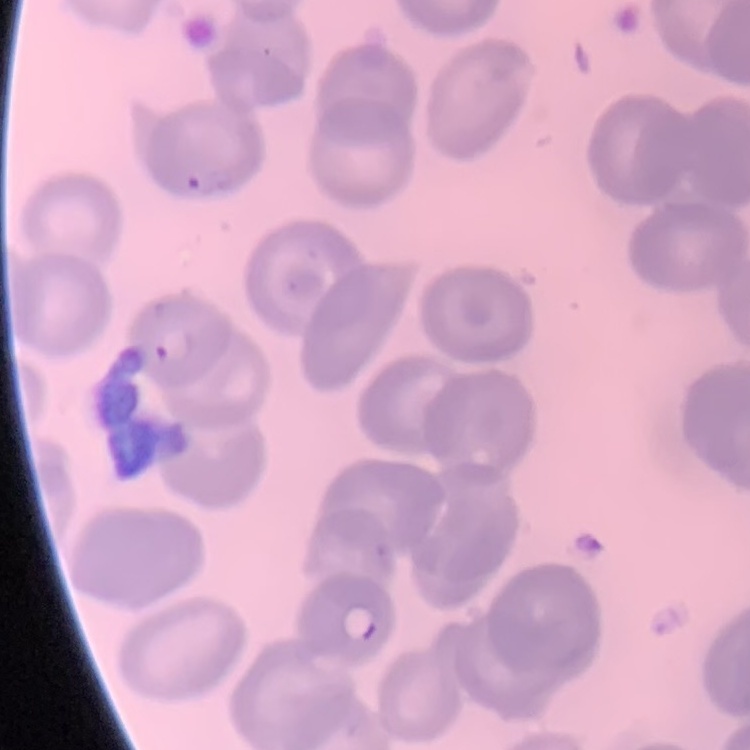
red blood cell morphology = no rouleaux formation
preparation = thin blood smear
stain = Field's or Giemsa
image type = square crop of a larger photomicrograph